Give the extent of all Plasmodium falciparum-infected red blood cells.
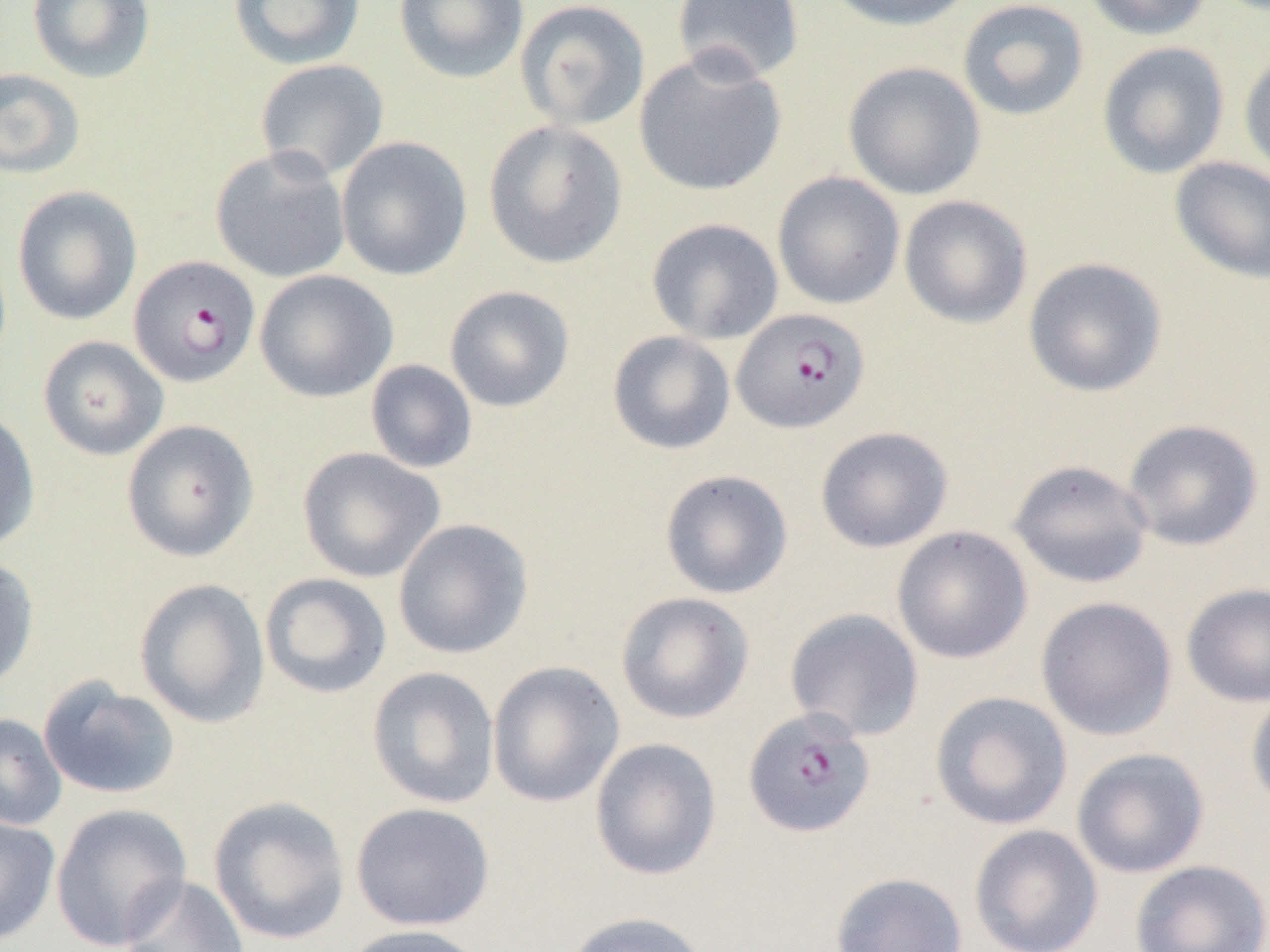
Approximate bounding boxes as (x1, y1, x2, y2) in pixels.
Plasmodium falciparum-infected red blood cells: (128, 255, 260, 387), (731, 307, 871, 433), (743, 706, 877, 838).

Summary:
  - Uninfected red blood cell locations: (26, 0, 155, 83), (229, 0, 366, 69), (394, 0, 530, 85), (671, 0, 806, 85), (821, 0, 980, 32), (957, 0, 1089, 122), (1081, 0, 1214, 41), (514, 1, 651, 131), (1097, 41, 1230, 179), (633, 49, 788, 197), (1239, 51, 1270, 181), (255, 59, 389, 182), (842, 61, 986, 200), (0, 67, 86, 179), (483, 120, 628, 269), (335, 136, 473, 281), (210, 146, 351, 283), (1169, 156, 1270, 285), (772, 171, 905, 310), (12, 186, 142, 326), (898, 195, 1033, 329), (646, 218, 784, 345), (1022, 257, 1168, 398), (254, 269, 398, 402), (444, 285, 575, 412), (607, 330, 736, 455), (37, 335, 169, 461), (365, 359, 478, 474), (0, 408, 41, 552), (1121, 418, 1264, 552), (121, 419, 259, 562), (815, 426, 954, 553), (297, 447, 445, 583), (1008, 459, 1154, 589), (659, 469, 794, 599), (393, 518, 534, 660), (891, 526, 1032, 664), (0, 554, 39, 692), (259, 572, 393, 699), (134, 578, 271, 728), (1181, 583, 1270, 707), (615, 591, 755, 724), (1035, 596, 1178, 741), (784, 607, 924, 742), (487, 661, 625, 808), (366, 666, 500, 809), (37, 676, 182, 800), (1246, 687, 1270, 812), (929, 690, 1073, 830), (0, 713, 67, 832), (589, 737, 722, 880), (1071, 747, 1210, 878), (207, 796, 351, 945), (49, 802, 192, 951), (350, 802, 496, 931), (0, 815, 61, 946), (969, 824, 1104, 952), (1130, 859, 1270, 952), (830, 871, 968, 952), (119, 874, 250, 952), (560, 911, 710, 952), (339, 924, 491, 952)
  - Slide-level diagnosis: Plasmodium falciparum
  - Image size: 1270×952 pixels
  - Preparation: thin blood smear
  - Field of view: single
  - Modality: optical microscopy
  - Magnification: 1000x